Report the malaria status of this cell.
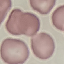
Uninfected.

Summary:
  - Preparation: thin blood smear
  - Stain: Giemsa
  - Image type: automatically extracted cell patch, resized to 64 × 64 pixels
  - Capture: smartphone camera at the microscope eyepiece